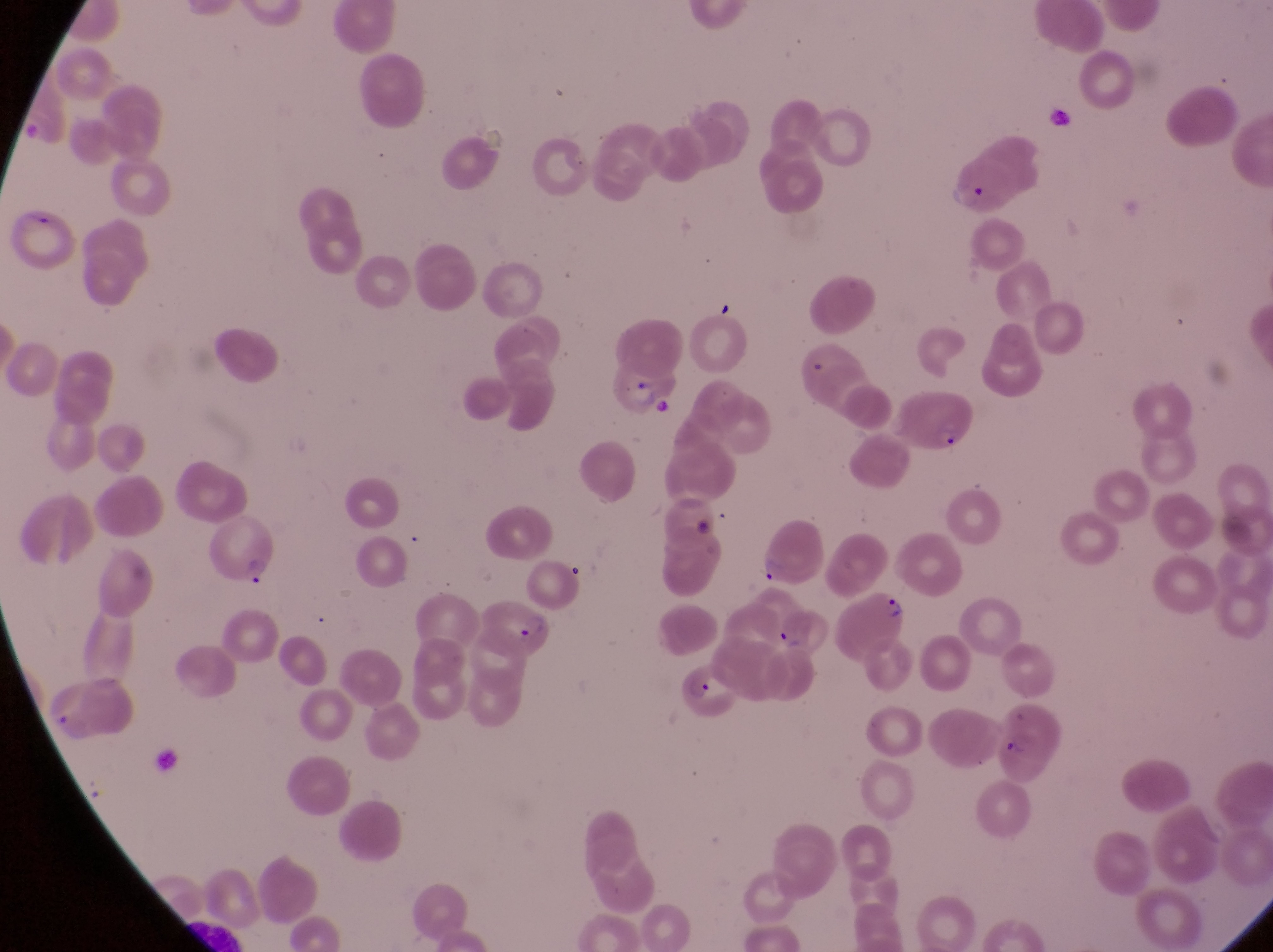

{
  "preparation": "thin blood smear",
  "field_of_view": "single",
  "capture": "smartphone photograph through the eyepiece of an Olympus CX-23 microscope",
  "magnification": "1000x",
  "country": "Uganda",
  "image_size": "1273×952 pixels",
  "parasitised_red_blood_cell_locations": "approximate bounding boxes as left top right bottom in pixels: 948 150 1018 212; 5 199 68 271; 611 360 669 420; 893 385 978 459; 200 519 272 586; 839 586 908 671; 482 600 552 657; 774 609 832 664; 684 661 747 726; 995 726 1055 786"
}